Comment on the morphology of the erythrocytes.
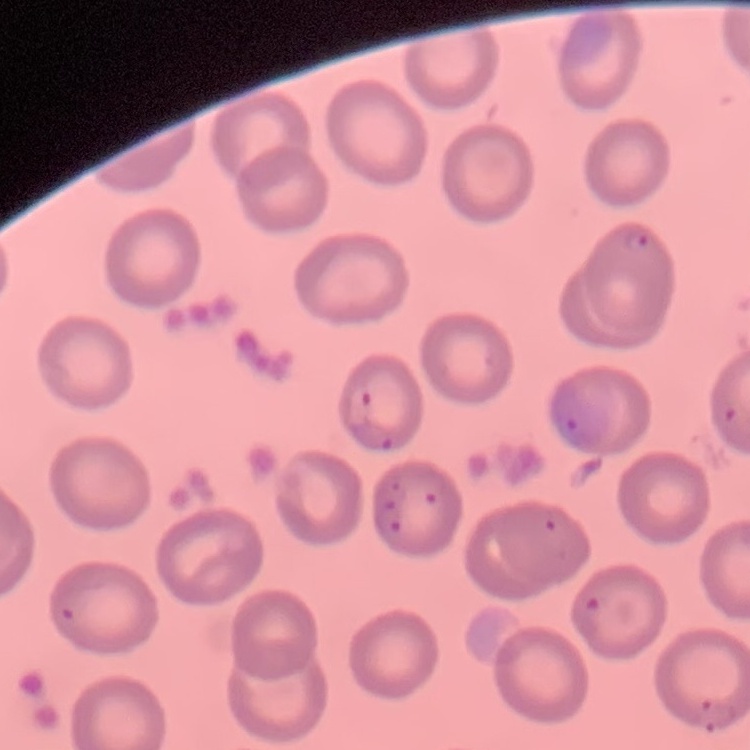

They show no rouleaux formation.

image type = square crop of a larger photomicrograph
stain = Field's or Giemsa
preparation = thin peripheral smear